State the preparation type.
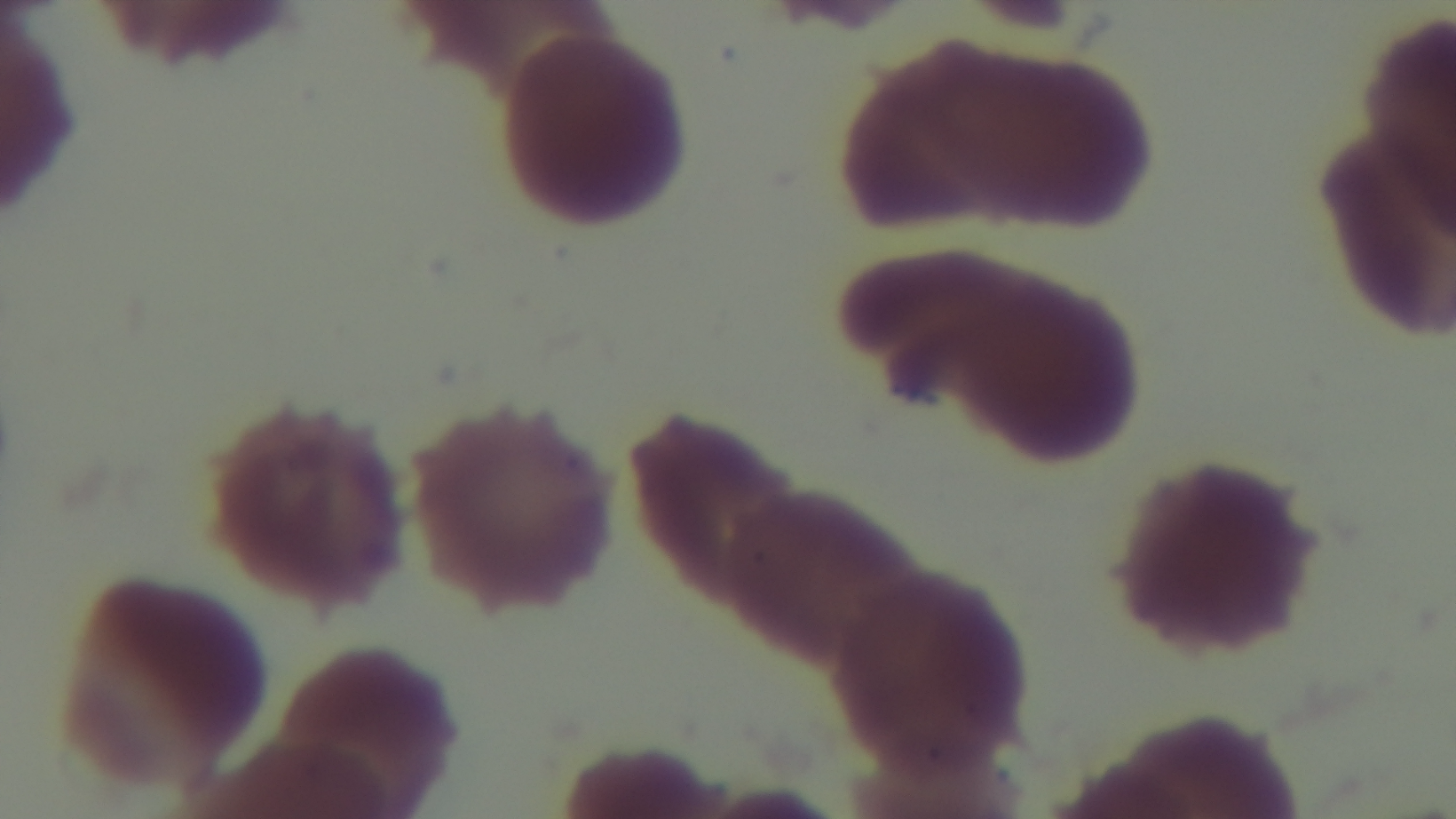

A thin smear.

field_of_view: one from the slide
modality: light microscopy
stain: Giemsa
objective: 100x oil immersion
capture: mounted 4K digital camera
malaria_status: uninfected